Locate every parasitized RBC.
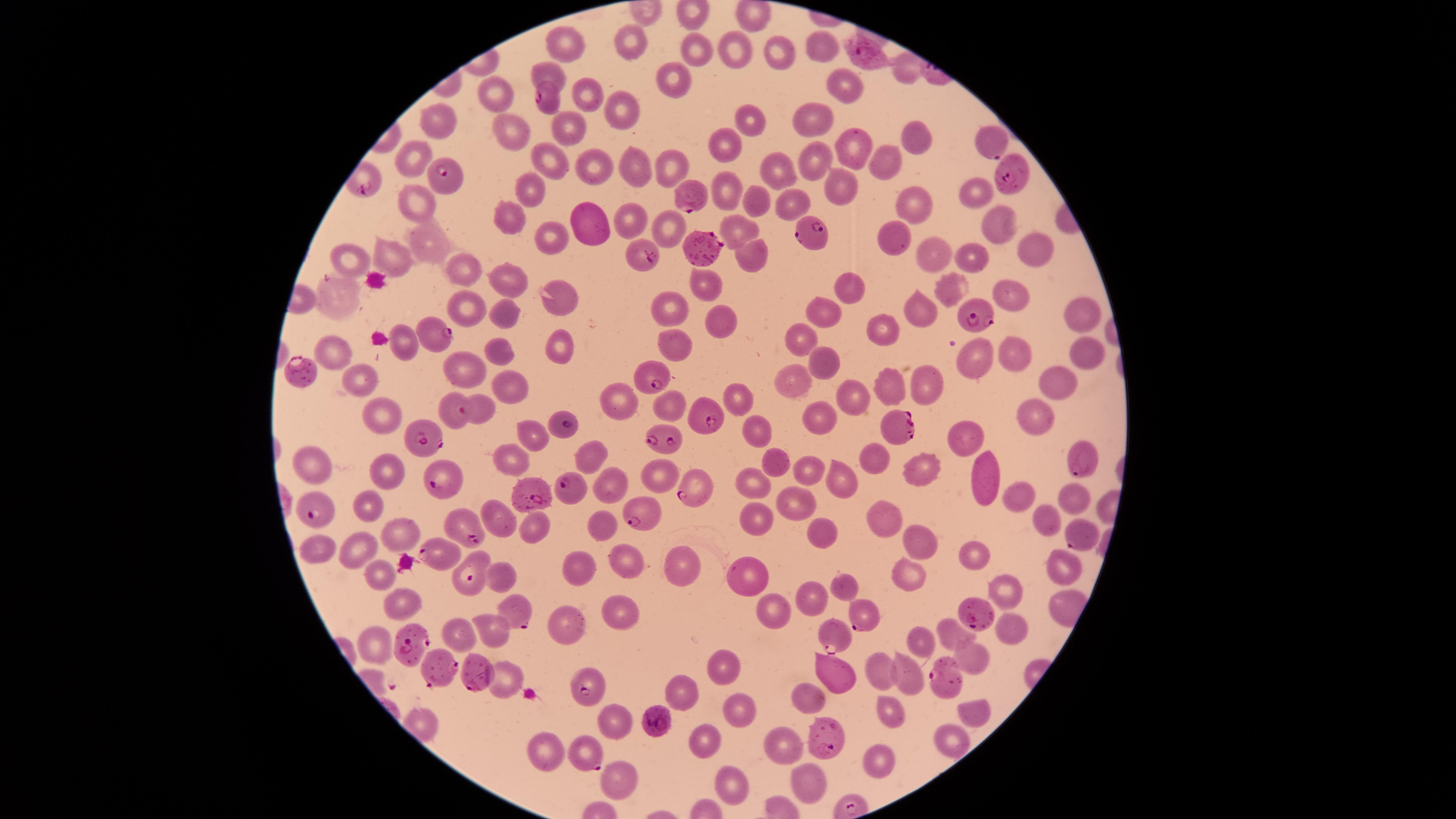

Approximate marker points as {x, y} in pixels.
Parasitized RBCs: {865, 58}, {548, 100}, {991, 142}, {445, 173}, {1012, 177}, {691, 195}, {808, 233}, {707, 246}, {641, 256}, {978, 314}, {436, 331}, {300, 367}, {647, 373}, {457, 412}, {710, 419}, {565, 424}, {903, 424}, {661, 437}, {421, 438}, {1078, 461}, {438, 480}, {565, 485}, {690, 491}, {528, 498}, {316, 514}, {640, 517}, {467, 528}, {1077, 535}, {433, 552}, {466, 578}, {977, 612}, {513, 613}, {857, 615}, {827, 639}, {407, 645}, {474, 674}, {440, 675}, {946, 675}, {589, 688}, {662, 720}, {821, 735}, {588, 756}.

Approximate marker points as {x, y} in pixels.
Summary:
  - Uninfected RBCs: {631, 41}, {819, 45}, {566, 46}, {696, 47}, {734, 48}, {779, 53}, {904, 70}, {671, 80}, {840, 87}, {494, 94}, {587, 94}, {617, 106}, {745, 118}, {441, 120}, {814, 120}, {573, 131}, {506, 135}, {913, 136}, {848, 139}, {727, 143}, {668, 156}, {415, 160}, {590, 161}, {887, 162}, {554, 165}, {814, 166}, {774, 168}, {635, 170}, {835, 180}, {535, 189}, {727, 189}, {975, 191}, {752, 197}, {419, 199}, {788, 204}, {917, 208}, {512, 214}, {993, 219}, {585, 222}, {630, 223}, {665, 228}, {741, 229}, {426, 235}, {546, 235}, {889, 236}, {936, 249}, {1034, 249}, {973, 250}, {393, 255}, {750, 256}, {347, 258}, {457, 264}, {506, 278}, {851, 283}, {708, 286}, {951, 287}, {1010, 293}, {335, 294}, {558, 302}, {468, 306}, {671, 309}, {825, 309}, {924, 311}, {1084, 312}, {500, 314}, {719, 324}, {885, 328}, {803, 340}, {404, 341}, {675, 341}, {556, 342}, {332, 348}, {1083, 350}, {1011, 352}, {499, 356}, {818, 360}, {975, 360}, {464, 370}, {1057, 377}, {363, 379}, {892, 381}, {799, 382}, {506, 383}, {924, 385}, {851, 394}, {740, 395}, {615, 399}, {671, 403}, {379, 411}, {819, 412}, {479, 415}, {1033, 415}, {528, 430}, {757, 431}, {965, 435}, {876, 455}, {593, 456}, {512, 459}, {774, 460}, {388, 467}, {923, 467}, {809, 469}, {321, 471}, {656, 471}, {983, 471}, {750, 478}, {841, 481}, {603, 483}, {1074, 494}, {796, 500}, {1020, 500}, {367, 502}, {1046, 516}, {751, 517}, {883, 517}, {504, 518}, {600, 523}, {527, 525}, {400, 529}, {820, 532}, {915, 537}, {314, 546}, {352, 547}, {625, 553}, {973, 554}, {1063, 564}, {583, 566}, {685, 570}, {741, 570}, {373, 572}, {502, 575}, {909, 576}, {846, 582}, {1005, 584}, {811, 593}, {402, 601}, {623, 609}, {777, 609}, {569, 626}, {1007, 628}, {459, 630}, {495, 631}, {956, 631}, {919, 641}, {375, 647}, {975, 656}, {723, 665}, {836, 672}, {882, 674}, {908, 676}, {501, 678}, {680, 691}, {811, 696}, {973, 709}, {738, 710}, {888, 714}, {614, 724}, {954, 735}, {708, 739}, {786, 748}, {546, 751}, {876, 755}, {805, 780}, {616, 783}, {729, 784}
  - Visible region: circular
  - Stain: Giemsa
  - Image size: 1456×819 pixels
  - Species: Plasmodium falciparum
  - Field of view: single
  - Preparation: thin blood film
  - Capture: smartphone photograph through the microscope eyepiece